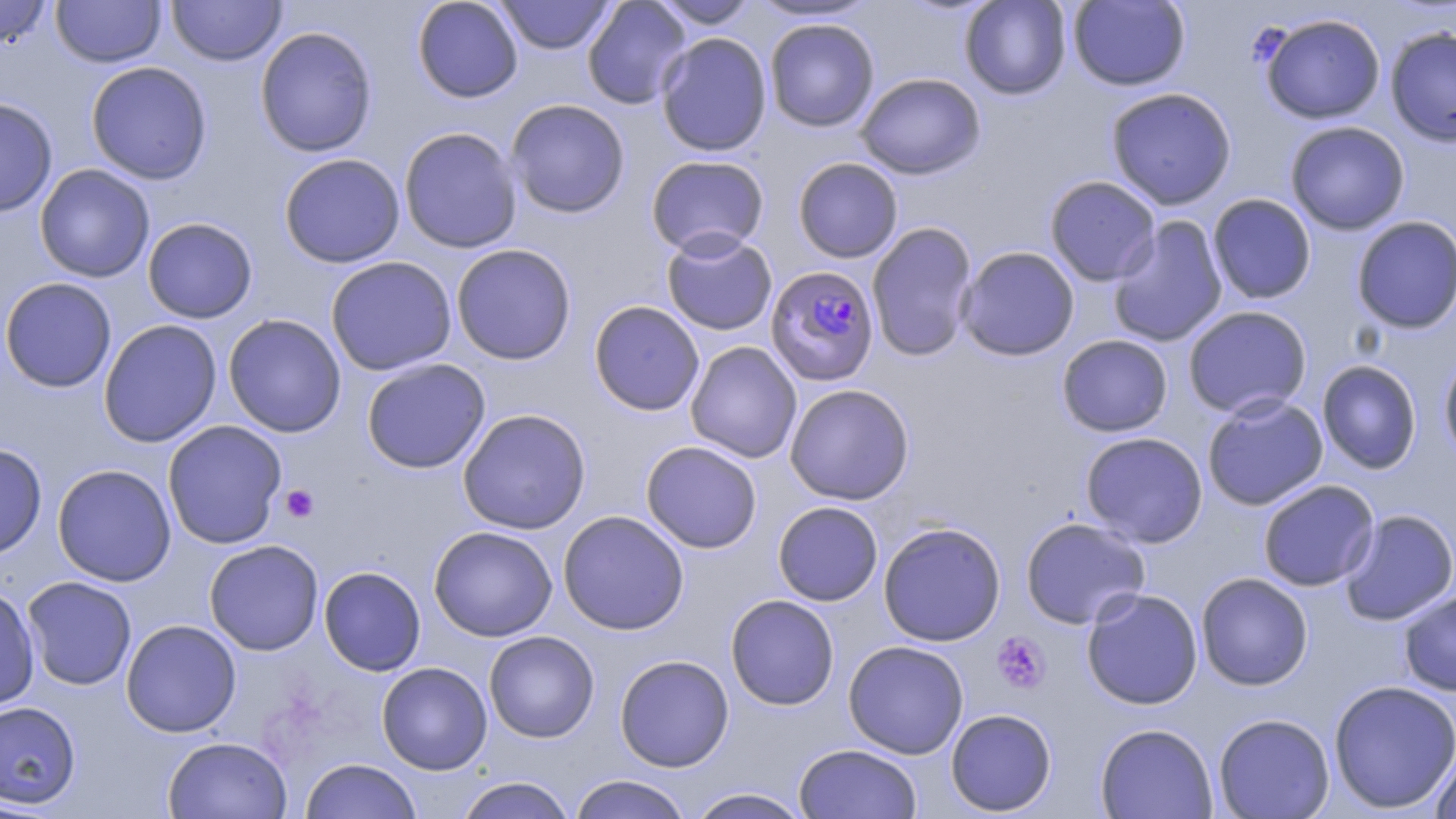
Summary:
  - Coordinate format: approximate bounding boxes as [x1, y1, x2, y2] in pixels
  - Uninfected red blood cell locations: [0, 0, 54, 50], [50, 0, 166, 68], [167, 0, 286, 66], [412, 0, 523, 103], [495, 0, 615, 55], [582, 0, 692, 109], [649, 0, 760, 29], [747, 0, 881, 23], [960, 0, 1071, 100], [1068, 0, 1189, 91], [1259, 13, 1385, 125], [764, 18, 879, 132], [254, 26, 378, 157], [1385, 26, 1456, 147], [656, 32, 772, 157], [85, 61, 213, 185], [855, 72, 986, 179], [1106, 87, 1237, 210], [0, 97, 58, 217], [505, 99, 631, 218], [1285, 121, 1410, 235], [398, 126, 523, 254], [278, 153, 406, 268], [645, 155, 769, 257], [792, 157, 903, 263], [34, 164, 155, 283], [1044, 175, 1161, 286], [1207, 193, 1316, 304], [1106, 216, 1228, 348], [1352, 216, 1456, 334], [142, 217, 258, 324], [866, 222, 978, 361], [661, 230, 777, 336], [451, 243, 577, 365], [956, 246, 1080, 360], [325, 256, 457, 376], [0, 277, 117, 393], [589, 300, 705, 416], [1182, 305, 1312, 419], [223, 313, 346, 437], [98, 319, 222, 448], [1056, 334, 1173, 437], [685, 341, 802, 463], [1439, 350, 1456, 466], [361, 358, 490, 474], [1317, 359, 1422, 474], [784, 384, 915, 505], [1202, 394, 1328, 511], [457, 407, 592, 535], [162, 420, 288, 549], [1080, 431, 1208, 548], [640, 440, 762, 553], [0, 442, 47, 561], [52, 464, 177, 586], [1257, 479, 1379, 592], [772, 501, 883, 606], [1338, 508, 1456, 625], [558, 510, 689, 635], [1020, 516, 1150, 629], [878, 521, 1006, 647], [428, 525, 558, 642], [204, 540, 324, 655], [319, 566, 426, 676], [1196, 572, 1313, 690], [21, 576, 137, 690], [0, 585, 40, 711], [1081, 588, 1203, 709], [1398, 588, 1456, 696], [725, 594, 839, 710], [120, 619, 242, 737], [483, 630, 599, 742], [843, 640, 969, 759], [614, 654, 734, 773], [376, 661, 492, 775], [1328, 679, 1456, 814], [0, 700, 81, 808], [945, 708, 1057, 816], [1213, 713, 1335, 818], [1095, 722, 1218, 818], [162, 736, 292, 818], [793, 743, 923, 819], [1430, 743, 1456, 819], [300, 758, 421, 819], [567, 774, 693, 819], [453, 777, 578, 818], [687, 787, 811, 818]
  - Plasmodium falciparum-infected red blood cell locations: [765, 265, 880, 387]
  - Platelet locations: [280, 484, 319, 523], [991, 632, 1051, 694]
  - Slide-level diagnosis: Plasmodium falciparum
  - Modality: optical microscopy
  - Stain: May-Grünwald-Giemsa
  - Preparation: thin blood film
  - Magnification: 1000x
  - Field of view: one of a larger specimen
  - Image size: 1456×819 pixels